Locate and identify every blood parasite.
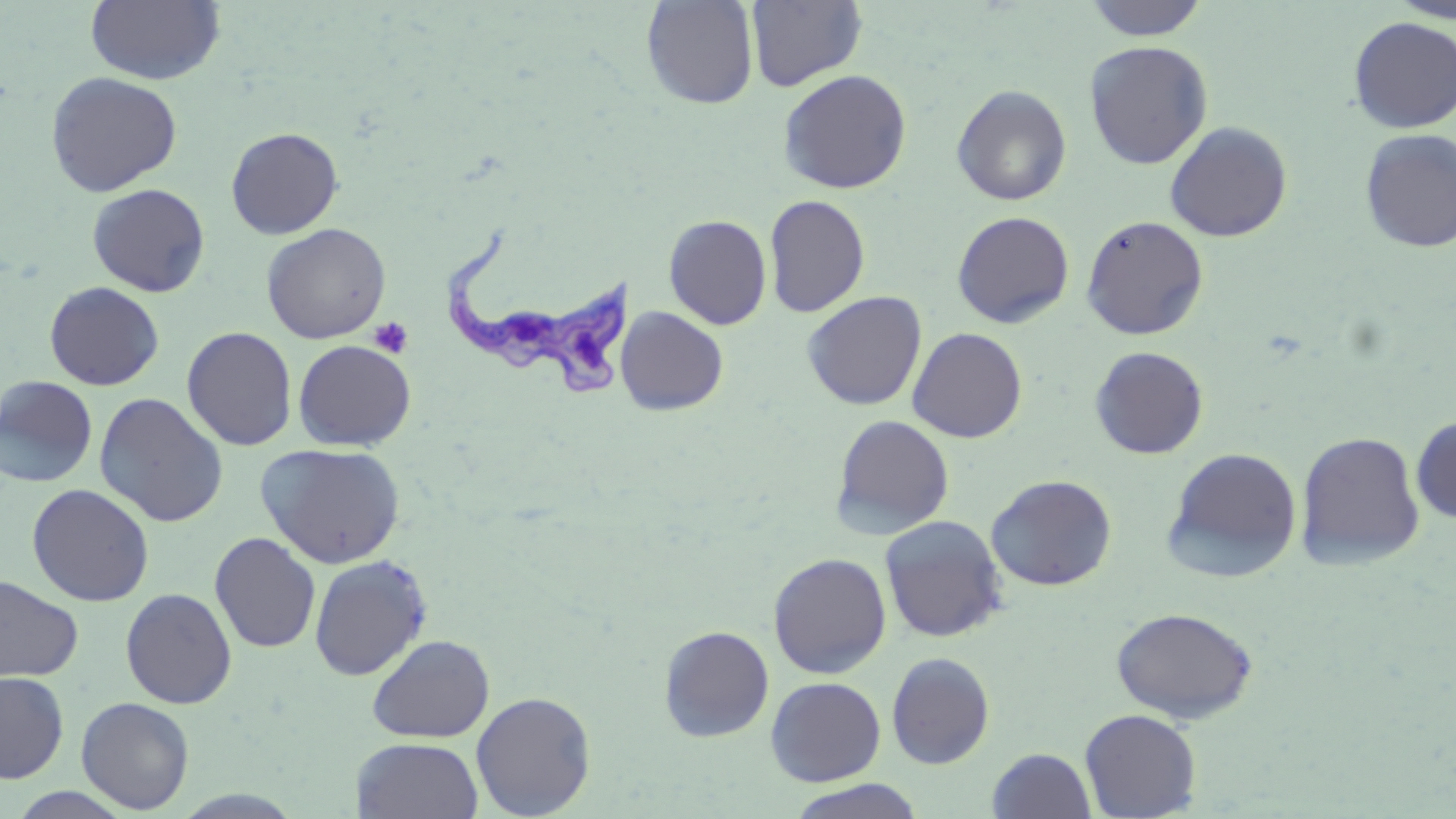

Approximate bounding boxes as [x1, y1, x2, y2] in pixels.
Trypanosoma brucei: [439, 229, 633, 400].
No Plasmodium falciparum, Plasmodium ovale, Plasmodium malariae, Plasmodium vivax, or Babesia divergens observed.

slide-level diagnosis = Trypanosoma brucei
stain = May-Grünwald-Giemsa
preparation = thin blood smear
uninfected red blood cell locations = approximate bounding boxes as [x1, y1, x2, y2] in pixels: [86, 0, 225, 86], [1083, 0, 1208, 41], [1388, 0, 1456, 23], [640, 1, 759, 109], [746, 1, 867, 91], [1348, 16, 1456, 134], [1084, 40, 1213, 169], [777, 69, 912, 194], [45, 71, 182, 197], [951, 84, 1072, 206], [1164, 121, 1292, 242], [225, 127, 344, 239], [1359, 128, 1456, 253], [87, 183, 210, 297], [764, 194, 870, 317], [952, 210, 1075, 328], [663, 214, 772, 330], [1080, 215, 1209, 340], [261, 223, 391, 343], [44, 281, 164, 391], [802, 291, 926, 410], [615, 306, 728, 415], [182, 326, 298, 451], [907, 327, 1028, 443], [292, 340, 416, 451], [1089, 346, 1209, 460], [0, 376, 98, 487], [94, 392, 229, 527], [831, 414, 955, 539], [1411, 416, 1456, 523], [1295, 430, 1425, 570], [256, 443, 406, 568], [1163, 447, 1302, 582], [985, 474, 1118, 591], [26, 483, 154, 607], [878, 514, 1009, 642], [209, 532, 321, 653], [768, 552, 892, 678], [308, 554, 433, 681], [0, 575, 83, 683], [120, 587, 237, 709], [1111, 606, 1259, 723], [658, 625, 774, 742], [367, 634, 495, 743], [886, 652, 995, 769], [0, 671, 69, 783], [765, 676, 886, 787], [471, 691, 596, 818], [76, 696, 194, 814], [1079, 708, 1202, 818], [352, 737, 483, 819], [986, 748, 1097, 819], [784, 779, 927, 819], [6, 787, 137, 819]
field of view = one of a larger specimen
image size = 1456×819 pixels
modality = light microscopy
platelet locations = approximate bounding boxes as [x1, y1, x2, y2] in pixels: [368, 316, 414, 359]
magnification = 1000x